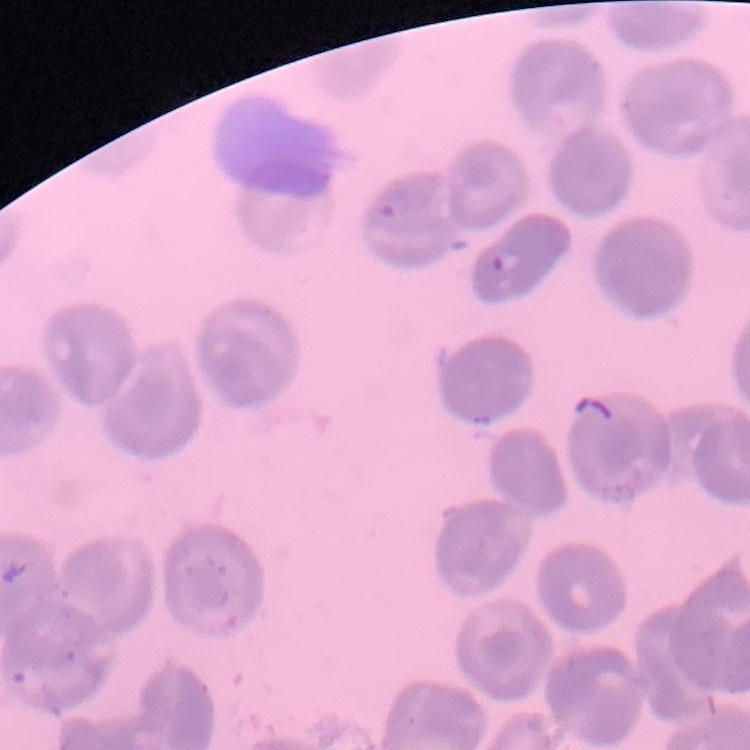

Summary:
  - Red blood cell morphology: no rouleaux formation
  - Stain: Field's or Giemsa
  - Preparation: thin blood smear
  - Image type: one tile cut from a larger photomicrograph